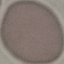

result = no malaria parasites detected
image type = cell patch, automatically extracted from a larger field of view and resized to 64 × 64 pixels
capture = smartphone camera at the microscope eyepiece
stain = Giemsa
preparation = thin smear